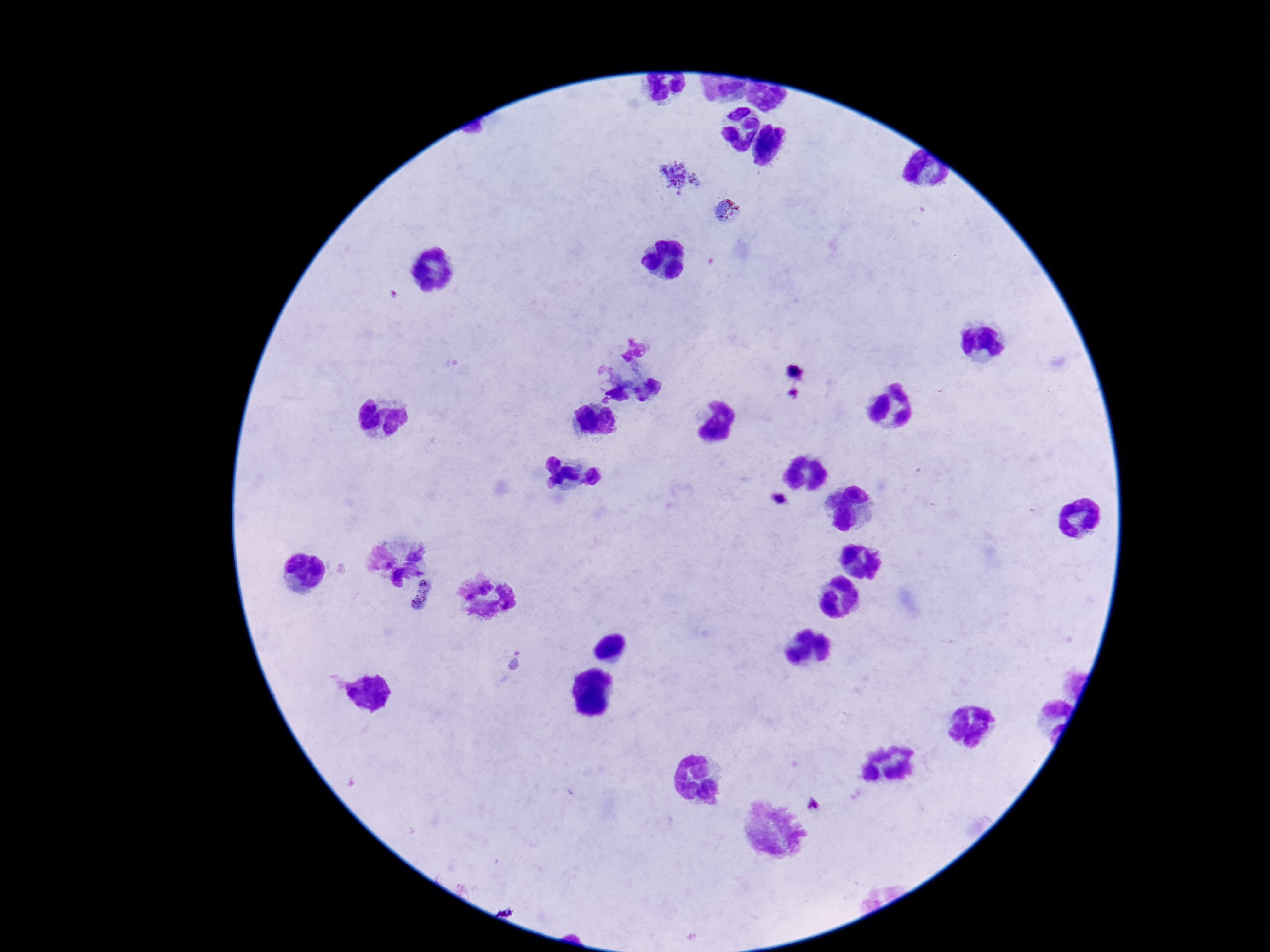 Approximate centers as (x, y) in pixels. Plasmodium parasite locations: (679, 177), (729, 211), (795, 371), (795, 393), (421, 596). Single field of view. Image is 1270×952 pixels. Patient malaria status: positive. Giemsa-stained preparation. Photographed through the microscope eyepiece with a smartphone camera. 100x magnification. Thick blood film.